Classify this cell by malaria status.
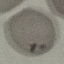
Uninfected.

Acquired by smartphone through the microscope eyepiece. Thin smear of blood. Cell patch, automatically extracted from a larger field of view and resized to 64 × 64 pixels. Giemsa-stained preparation.